Locate every malaria parasite.
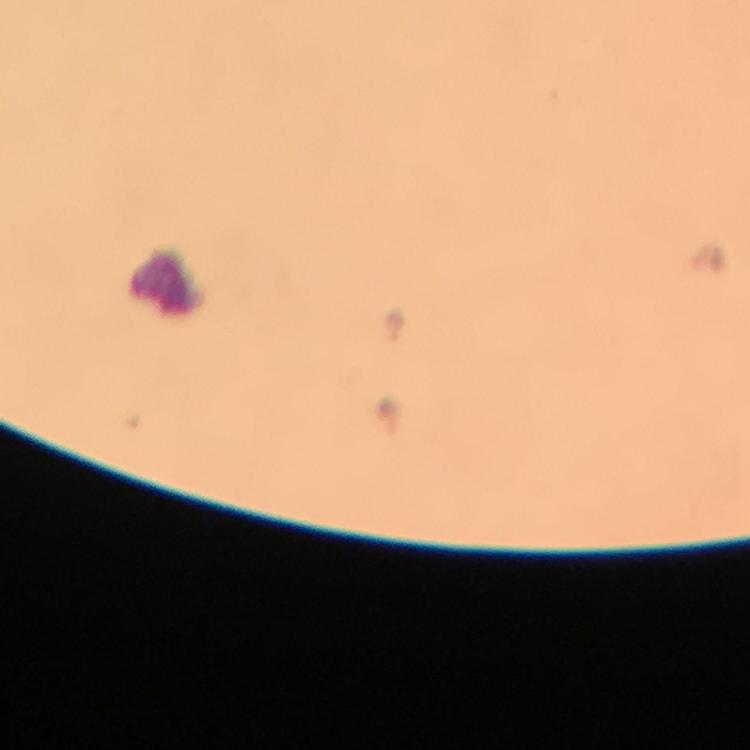

Approximate object centers, in pixels from the top-left corner.
Malaria parasites: (x=393, y=327).

{
  "capture": "smartphone camera through the microscope",
  "immersion_oil": "used",
  "preparation": "thick blood smear",
  "context": "from a diagnostic examination for malaria",
  "image_size": "750×750 pixels",
  "magnification": "100x",
  "stain": "Giemsa",
  "cropped_from": "a single field of view"
}